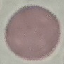
Malaria status: uninfected. Automatically extracted cell patch, resized to 64 × 64 pixels. Photographed with a smartphone camera at the microscope eyepiece. Thin smear of blood. Giemsa-stained preparation.